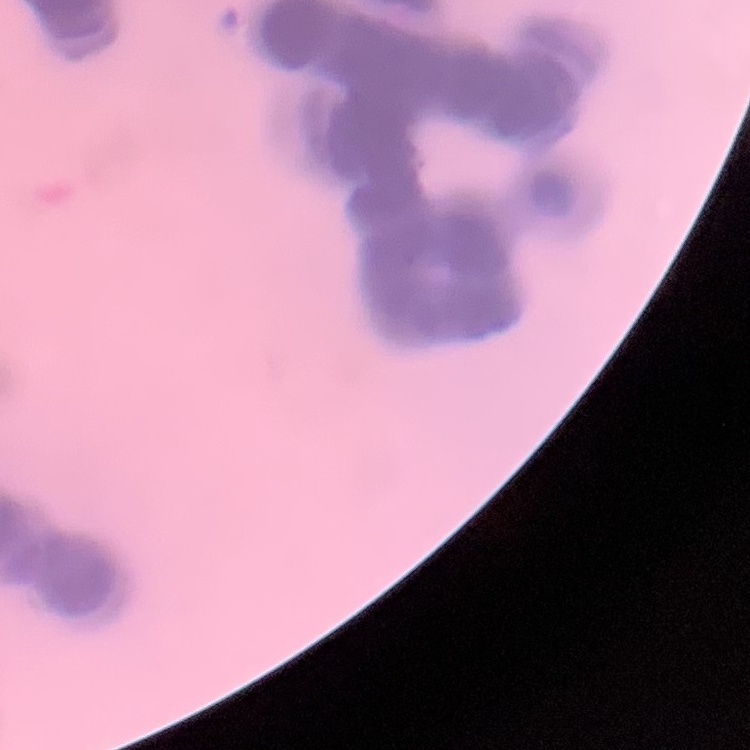
Summary:
  - Red blood cell morphology: rouleaux formation
  - Preparation: thin blood film
  - Stain: Field's or Giemsa
  - Image type: one tile cut from a larger photomicrograph